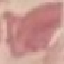 Malaria status: uninfected. Giemsa-stained preparation. Automatically extracted cell patch, resized to 64 × 64 pixels. Thin blood smear. Photographed with a smartphone camera at the microscope eyepiece.